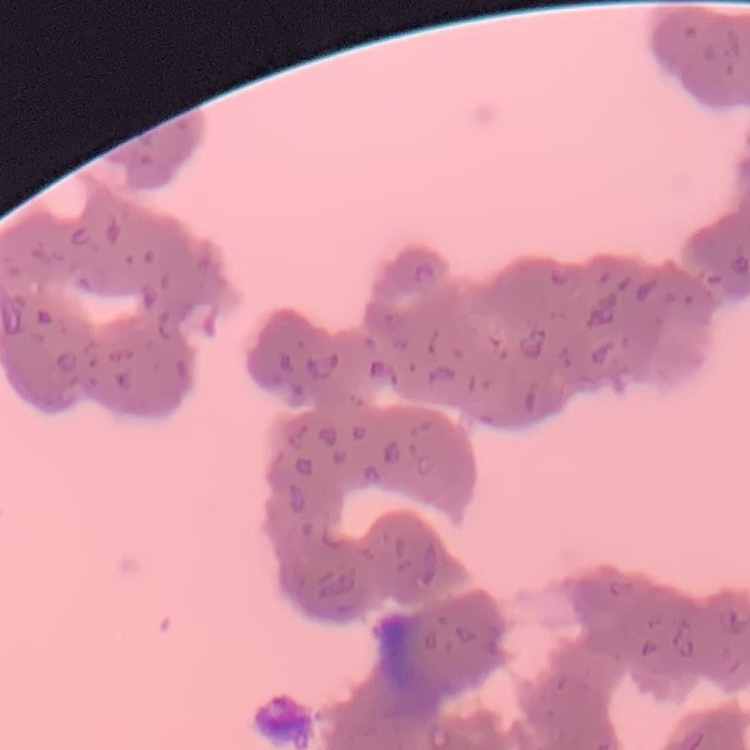
{
  "erythrocyte_morphology": "rouleaux formation",
  "preparation": "thin blood film",
  "image_type": "square crop of a larger photomicrograph",
  "stain": "Field's or Giemsa"
}